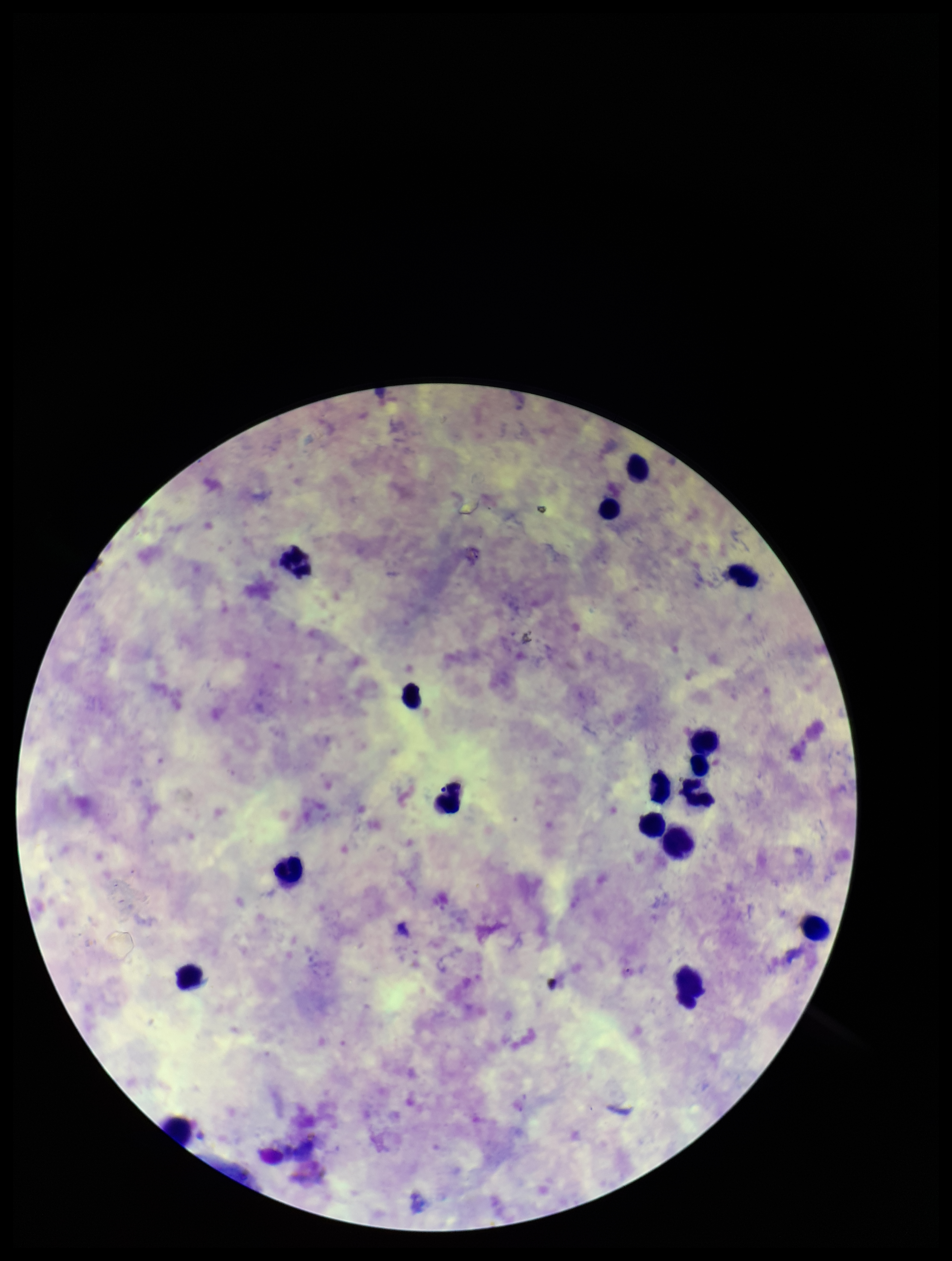

{
  "stain": "Giemsa",
  "leukocyte_count": 17,
  "plasmodium_parasites": "none identified",
  "preparation": "thick blood smear",
  "capture": "smartphone photograph through the microscope eyepiece",
  "parasite_count": 0,
  "patient_malaria_status": "infected",
  "field_of_view": "single",
  "image_size": "952×1261 pixels",
  "species_reported_for_this_patient": "Plasmodium vivax"
}